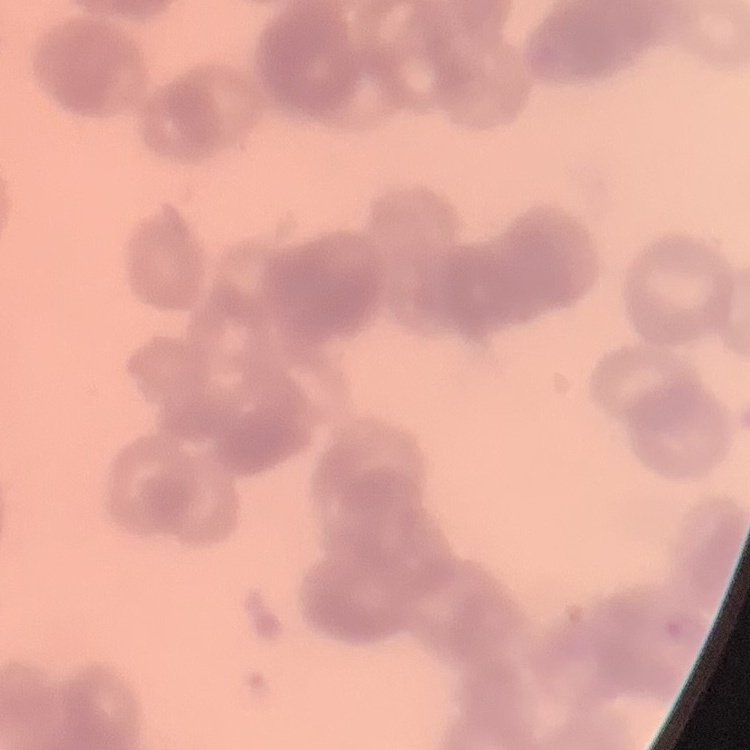
Summary:
  - Erythrocyte morphology: rouleaux formation
  - Stain: Field's or Giemsa
  - Image type: square crop of a larger photomicrograph
  - Preparation: thin blood smear